Assess this cell for malaria.
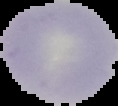
It is parasitized.

{
  "image_type": "cell region segmented out of the field of view; surrounding area masked to black",
  "preparation": "thin blood smear",
  "image_size": "118×106 pixels"
}